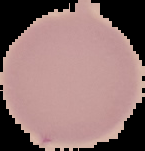

Summary:
  - Preparation: thin blood film
  - Malaria status: uninfected
  - Image type: segmented cell region on a black background
  - Image size: 145×151 pixels